Report the malaria status of this cell.
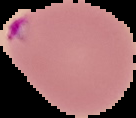
Parasitized.

Summary:
  - Preparation: thin blood film
  - Image type: segmented cell region with the area outside set to black
  - Image size: 136×118 pixels